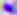
Captured at 400x magnification. Micrograph. Toxoplasma gondii is shown.